Locate every blood parasite and identify its species.
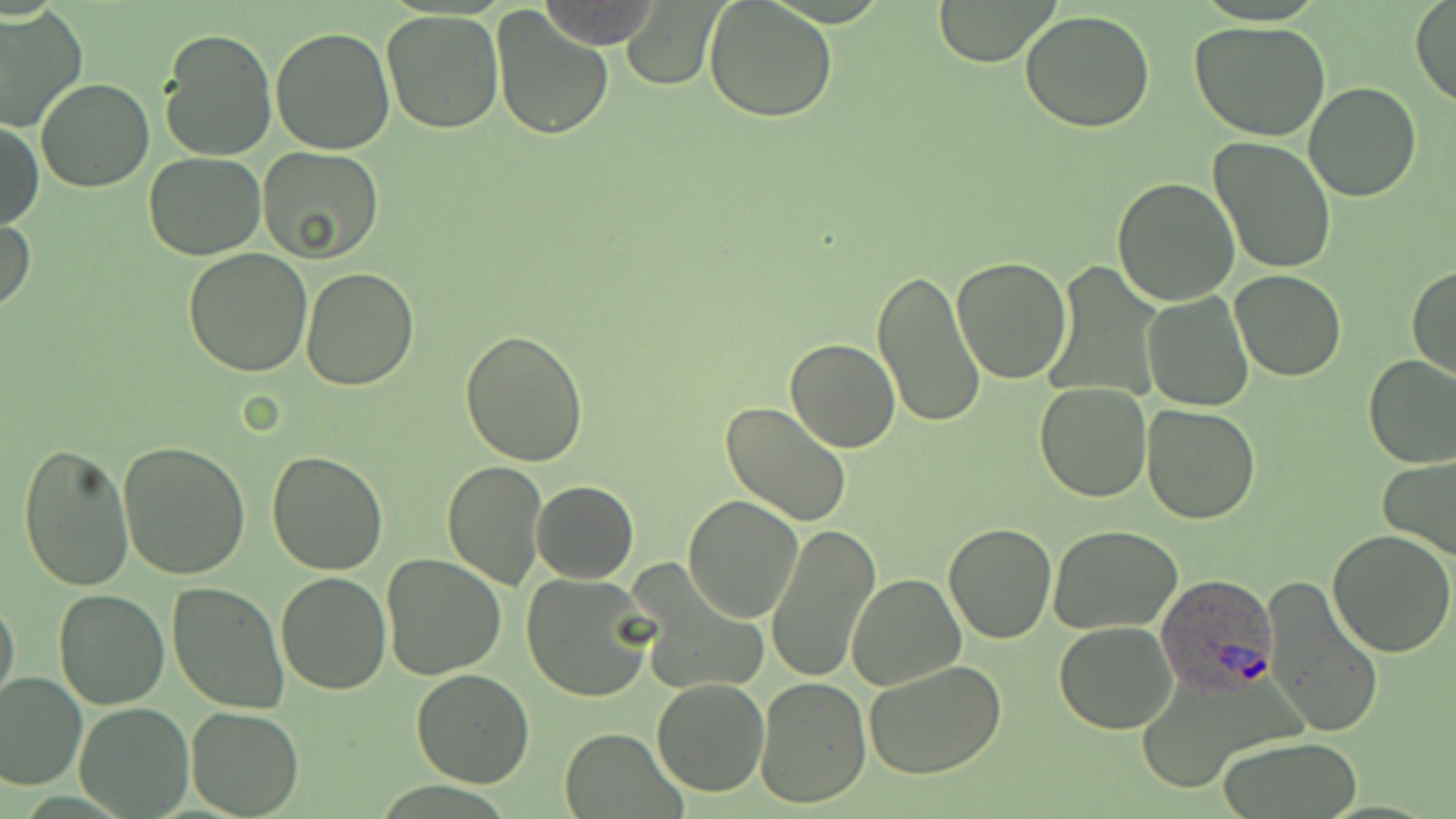

Approximate bounding boxes as [x1, y1, x2, y2] in pixels.
Plasmodium ovale-infected red blood cells: [1154, 573, 1279, 695].
No Plasmodium falciparum, Plasmodium malariae, Plasmodium vivax, Babesia divergens, or Trypanosoma brucei observed.

slide_level_diagnosis: Plasmodium ovale
uninfected_red_blood_cell_locations: 'approximate bounding boxes as [x1, y1, x2, y2] in pixels: [538, 0, 663, 48], [932, 0, 1058, 66], [704, 1, 839, 121], [1409, 1, 1455, 108], [622, 2, 721, 89], [492, 5, 615, 139], [0, 7, 86, 132], [380, 9, 505, 133], [1020, 11, 1155, 132], [1188, 21, 1331, 140], [270, 26, 397, 156], [157, 27, 278, 162], [36, 78, 154, 192], [1304, 81, 1421, 201], [1, 120, 43, 231], [1208, 137, 1336, 274], [257, 145, 384, 262], [143, 152, 266, 260], [1113, 176, 1241, 304], [0, 212, 35, 315], [184, 248, 313, 375], [951, 257, 1072, 386], [1406, 263, 1456, 382], [300, 266, 418, 390], [871, 267, 985, 427], [1231, 269, 1346, 381], [1143, 291, 1254, 412], [460, 329, 590, 466], [785, 339, 899, 453], [1364, 356, 1456, 470], [1033, 382, 1153, 502], [720, 402, 853, 527], [1141, 404, 1260, 524], [117, 441, 252, 579], [18, 443, 134, 592], [265, 451, 390, 576], [1379, 456, 1456, 560], [442, 458, 549, 590], [532, 481, 638, 582], [682, 494, 802, 624], [766, 522, 880, 685], [943, 522, 1057, 643], [1048, 524, 1183, 635], [1327, 530, 1456, 659], [392, 551, 520, 790], [382, 554, 505, 679], [521, 573, 655, 703], [276, 574, 390, 694], [845, 575, 965, 691], [1262, 578, 1385, 741], [167, 583, 289, 716], [54, 589, 169, 709], [0, 593, 20, 709], [1054, 621, 1178, 733], [865, 659, 1008, 779], [0, 669, 86, 790], [410, 669, 535, 787], [754, 676, 871, 809], [652, 677, 769, 798], [75, 702, 193, 817], [187, 706, 304, 818], [557, 729, 685, 816], [1218, 736, 1363, 817]'
field_of_view: single
modality: light microscopy
stain: May-Grünwald-Giemsa
magnification: 1000x
image_size: 1456×819 pixels
preparation: thin blood film